Assess this cell for malaria.
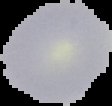

It is uninfected.

Segmented cell region on a black background. Image is 112×106 pixels. From a thin blood smear.